State which parasite is depicted.
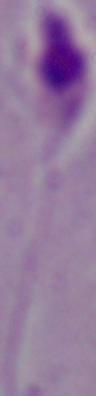
Leishmania.

Summary:
  - Modality: photomicrograph
  - Magnification: 1000x